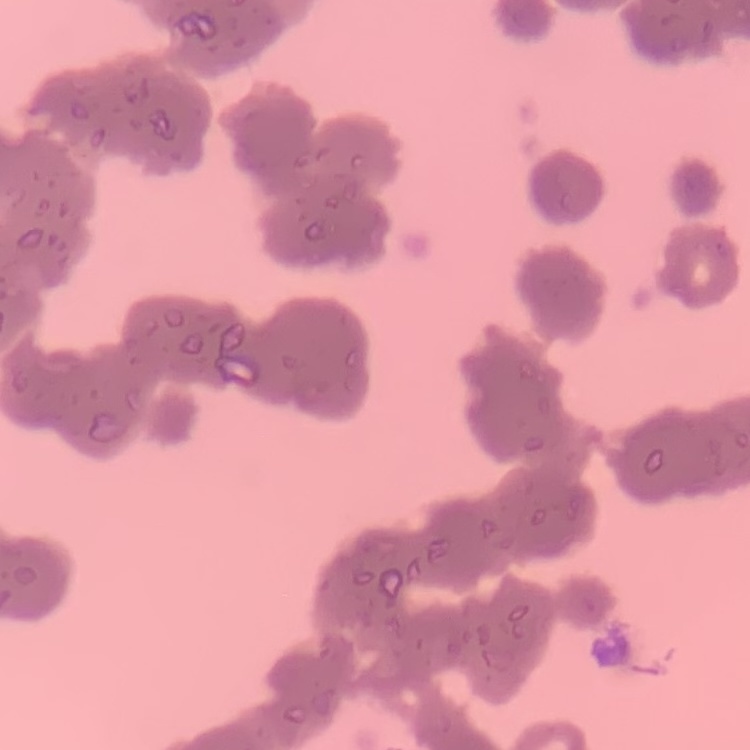
The red blood cells exhibit rouleaux formation. Square crop of a larger photomicrograph. Thin blood smear. Field's or Giemsa stain.